Identify the parasite.
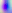
This is Toxoplasma gondii.

magnification = 400x
modality = photomicrograph